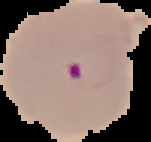
image size = 151×142 pixels
image type = segmented cell region on a black background
result = Plasmodium parasites identified
preparation = thin blood film